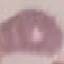

result: no malaria parasites detected
image_type: automatically extracted cell patch, resized to 64 × 64 pixels
capture: smartphone through the microscope eyepiece
stain: Giemsa
preparation: thin blood film